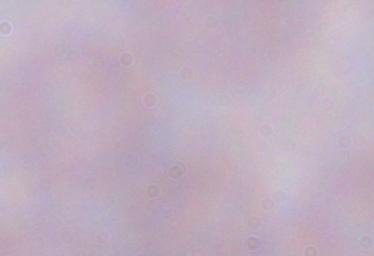
Micrograph. A trypanosome is seen. Captured at 1000x magnification.